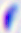
modality: photomicrograph
magnification: 400x
identification: Toxoplasma gondii